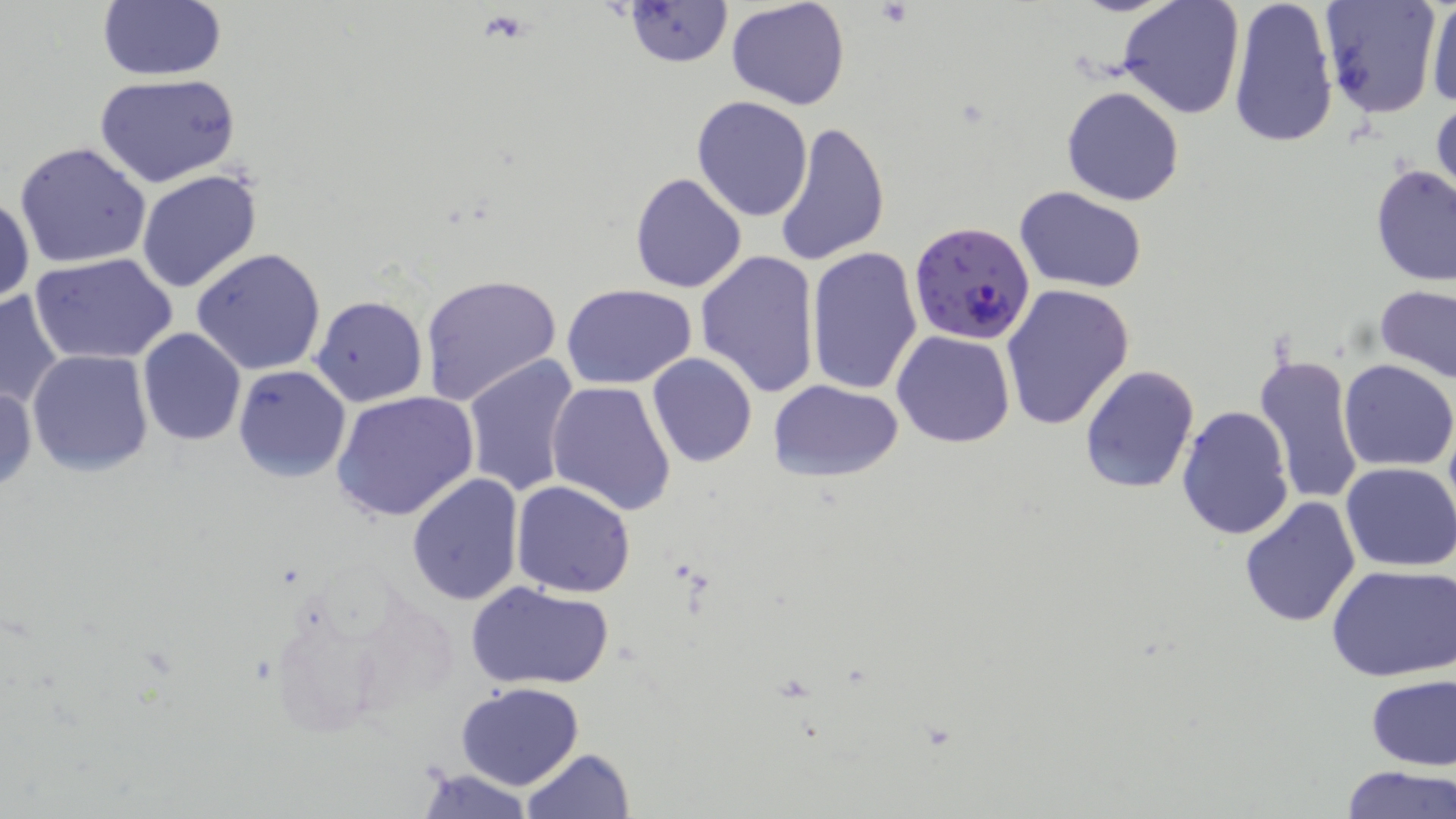 Approximate bounding boxes as [x1, y1, x2, y2] in pixels. Platelet locations: [876, 3, 915, 27], [479, 10, 530, 44]. Uninfected red blood cell locations: [623, 0, 732, 67], [725, 0, 850, 111], [1119, 0, 1246, 121], [1226, 0, 1342, 150], [1318, 0, 1443, 119], [1424, 0, 1456, 111], [95, 1, 227, 83], [1086, 31, 1241, 178], [95, 74, 241, 187], [1060, 85, 1186, 207], [692, 96, 813, 222], [1430, 99, 1456, 210], [773, 118, 892, 267], [14, 141, 153, 268], [1370, 165, 1455, 287], [136, 169, 264, 294], [628, 171, 748, 294], [1014, 186, 1148, 293], [0, 194, 35, 306], [806, 247, 925, 397], [191, 248, 329, 376], [695, 250, 822, 399], [31, 253, 178, 365], [419, 273, 562, 405], [559, 283, 698, 387], [1001, 284, 1134, 430], [1376, 286, 1456, 383], [0, 289, 66, 411], [311, 294, 429, 407], [137, 329, 246, 446], [892, 330, 1016, 447], [26, 349, 154, 477], [1253, 350, 1366, 509], [461, 352, 581, 499], [646, 354, 758, 470], [1338, 358, 1455, 471], [233, 364, 351, 483], [1079, 364, 1200, 496], [768, 379, 903, 482], [546, 381, 677, 518], [0, 383, 36, 492], [333, 390, 481, 522], [1176, 404, 1293, 543], [1340, 463, 1456, 571], [406, 474, 525, 608], [511, 480, 637, 598], [1239, 496, 1363, 628], [1327, 563, 1456, 681], [466, 580, 616, 690], [265, 594, 396, 741], [1364, 673, 1454, 771], [455, 681, 584, 789], [521, 747, 634, 818], [1338, 765, 1454, 819], [413, 769, 537, 818]. Plasmodium falciparum-infected red blood cell locations: [909, 219, 1036, 346]. Slide-level diagnosis: Plasmodium falciparum. One field of a larger specimen. Light microscopy. May-Grünwald-Giemsa-stained preparation. Thin blood smear. Image is 1456×819 pixels. Captured at 1000x magnification.